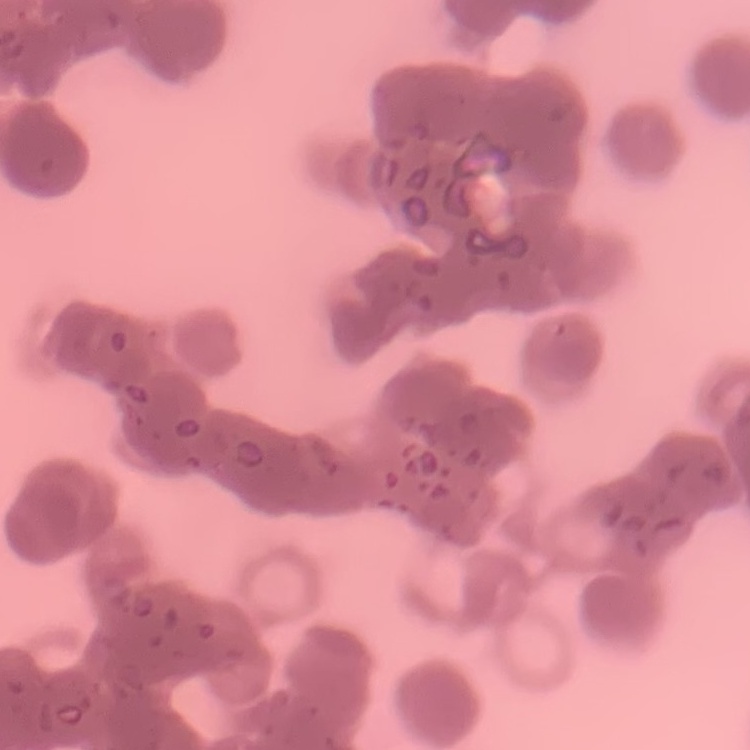

The erythrocytes show rouleaux formation. One tile cut from a larger photomicrograph. Thin peripheral smear. Field's or Giemsa stain.